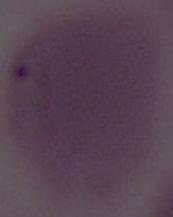

Photomicrograph. Captured at 1000x magnification. An erythrocyte is shown.